State which parasite is depicted.
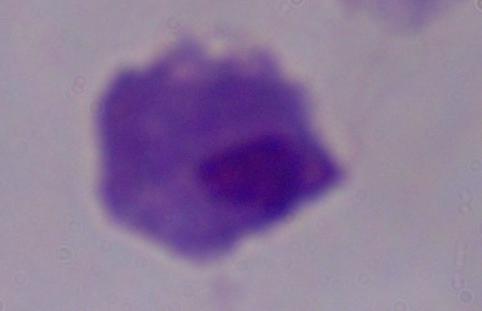
A trichomonad.

1000x magnification. Micrograph.